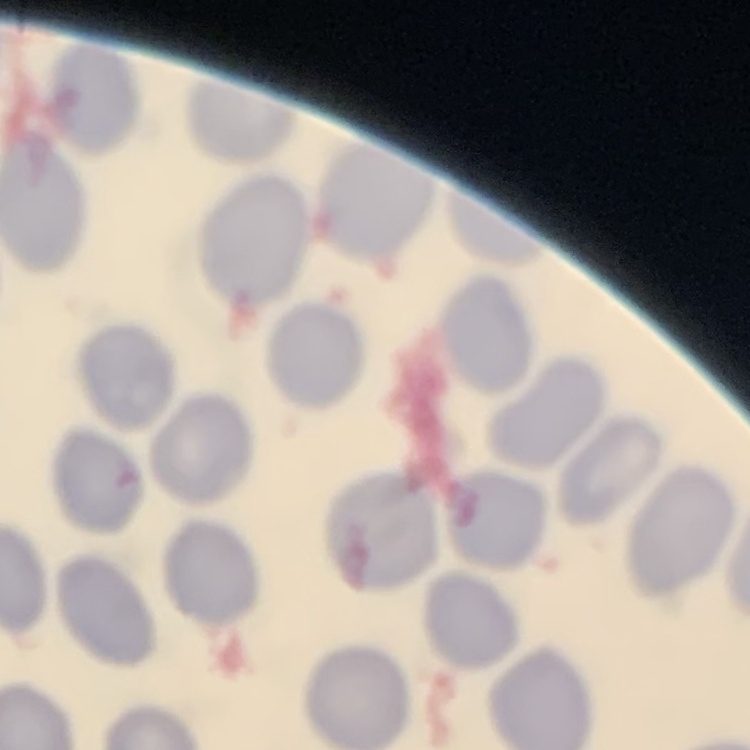

The erythrocytes exhibit no rouleaux formation. Stained with either Field's or Giemsa. Thin blood smear. Square crop of a larger photomicrograph.